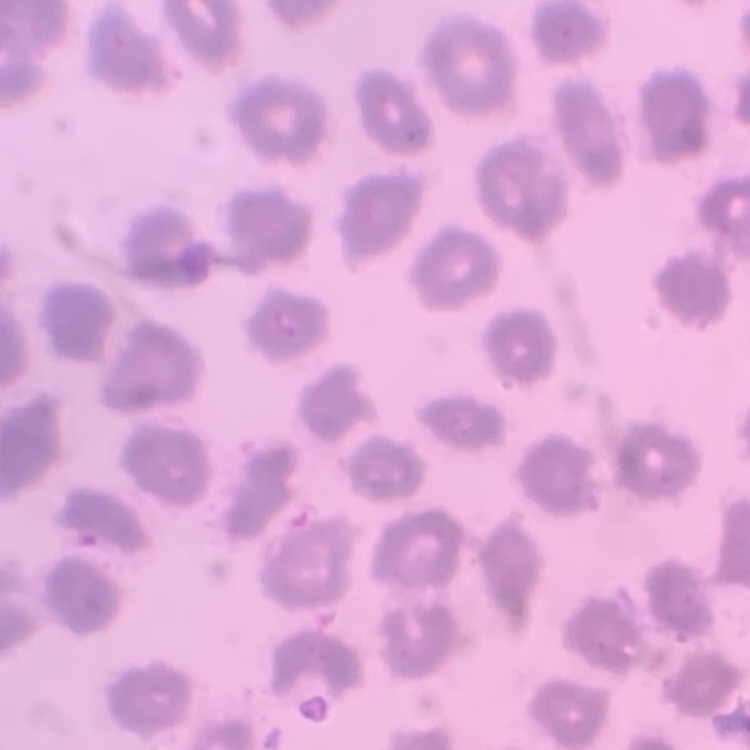

The red blood cells exhibit no rouleaux formation. One tile cut from a larger photomicrograph. Thin blood smear. Field's or Giemsa stain.